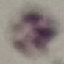

Malaria status: uninfected. Thin blood film. Automatically extracted cell patch, resized to 64 × 64 pixels. Photographed with a smartphone camera at the microscope eyepiece. Giemsa-stained preparation.